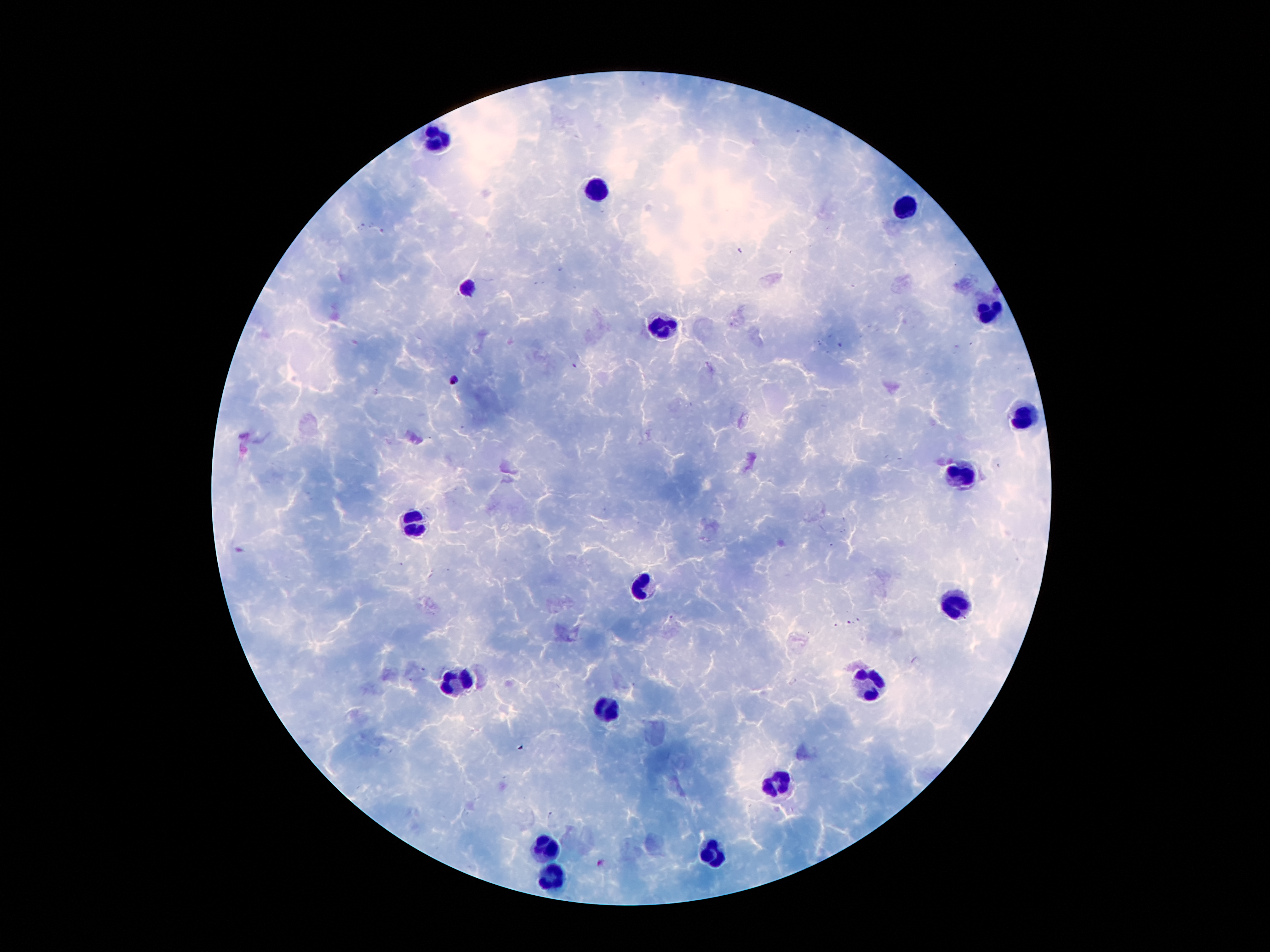
magnification: 100x
capture: smartphone camera through the microscope eyepiece
stain: Giemsa
image_size: 1270×952 pixels
leukocyte_locations: 'approximate centers as (x, y) in pixels: (436, 143), (594, 190), (903, 210), (469, 286), (989, 311), (665, 331), (1026, 417), (961, 481), (413, 526), (641, 587), (954, 601), (458, 679), (868, 683), (604, 712), (780, 783), (545, 847), (717, 853), (555, 884)'
preparation: thick blood smear
patient_malaria_status: infected with Plasmodium falciparum
field_of_view: one from this slide
plasmodium_parasite_locations: 'approximate centers as (x, y) in pixels: (574, 365), (455, 379), (858, 619), (849, 621), (836, 624), (600, 863)'